State the blood parasite species.
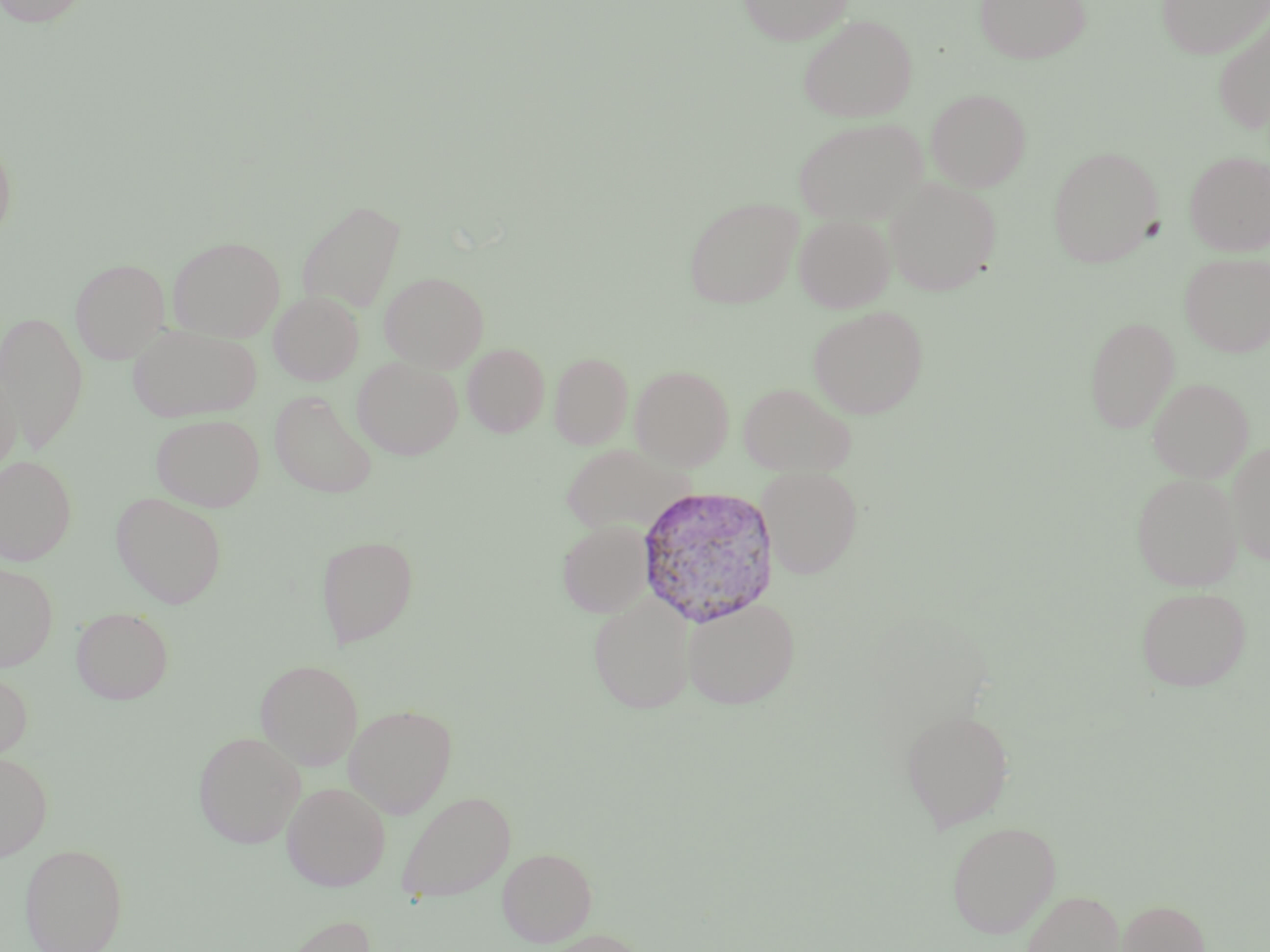

Plasmodium vivax.

Summary:
  - Coordinate format: approximate bounding boxes as named x1/y1/x2/y2 corners in pixels
  - Uninfected red blood cell locations: (x1=0, y1=0, x2=94, y2=27), (x1=737, y1=0, x2=853, y2=45), (x1=974, y1=0, x2=1092, y2=64), (x1=1156, y1=0, x2=1270, y2=59), (x1=797, y1=14, x2=918, y2=123), (x1=1211, y1=14, x2=1270, y2=133), (x1=925, y1=88, x2=1031, y2=192), (x1=793, y1=117, x2=927, y2=226), (x1=0, y1=131, x2=17, y2=243), (x1=1047, y1=146, x2=1162, y2=268), (x1=1183, y1=150, x2=1270, y2=256), (x1=883, y1=177, x2=1001, y2=297), (x1=684, y1=197, x2=803, y2=309), (x1=297, y1=199, x2=406, y2=314), (x1=793, y1=214, x2=895, y2=313), (x1=167, y1=236, x2=286, y2=342), (x1=1180, y1=252, x2=1270, y2=357), (x1=70, y1=258, x2=170, y2=364), (x1=380, y1=271, x2=489, y2=372), (x1=269, y1=291, x2=364, y2=385), (x1=808, y1=305, x2=929, y2=419), (x1=0, y1=310, x2=89, y2=454), (x1=1084, y1=316, x2=1180, y2=433), (x1=127, y1=325, x2=263, y2=422), (x1=462, y1=342, x2=550, y2=437), (x1=550, y1=352, x2=633, y2=449), (x1=352, y1=356, x2=463, y2=460), (x1=630, y1=365, x2=734, y2=469), (x1=0, y1=371, x2=23, y2=478), (x1=1148, y1=378, x2=1253, y2=482), (x1=738, y1=382, x2=856, y2=476), (x1=269, y1=390, x2=379, y2=498), (x1=151, y1=413, x2=265, y2=512), (x1=1226, y1=441, x2=1270, y2=565), (x1=561, y1=443, x2=689, y2=538), (x1=0, y1=455, x2=77, y2=565), (x1=757, y1=465, x2=864, y2=579), (x1=1131, y1=472, x2=1242, y2=590), (x1=111, y1=492, x2=228, y2=608), (x1=557, y1=518, x2=654, y2=618), (x1=316, y1=535, x2=420, y2=647), (x1=0, y1=562, x2=59, y2=671), (x1=1134, y1=586, x2=1251, y2=691), (x1=588, y1=592, x2=698, y2=713), (x1=682, y1=596, x2=801, y2=709), (x1=72, y1=607, x2=173, y2=705), (x1=255, y1=659, x2=364, y2=770), (x1=0, y1=668, x2=33, y2=762), (x1=344, y1=703, x2=458, y2=818), (x1=900, y1=708, x2=1015, y2=832), (x1=193, y1=731, x2=306, y2=849), (x1=0, y1=752, x2=53, y2=861), (x1=282, y1=781, x2=391, y2=891), (x1=396, y1=791, x2=514, y2=903), (x1=946, y1=820, x2=1061, y2=939), (x1=20, y1=844, x2=127, y2=952), (x1=497, y1=847, x2=597, y2=947), (x1=1021, y1=889, x2=1126, y2=952), (x1=1115, y1=899, x2=1210, y2=952), (x1=274, y1=914, x2=380, y2=952), (x1=536, y1=929, x2=649, y2=952)
  - Plasmodium vivax-infected red blood cell locations: (x1=635, y1=486, x2=781, y2=627)
  - Stain: May-Grünwald-Giemsa
  - Preparation: thin blood smear
  - Image size: 1270×952 pixels
  - Magnification: 1000x
  - Field of view: one of a larger specimen
  - Modality: optical microscopy